Give the position of every malaria parasite.
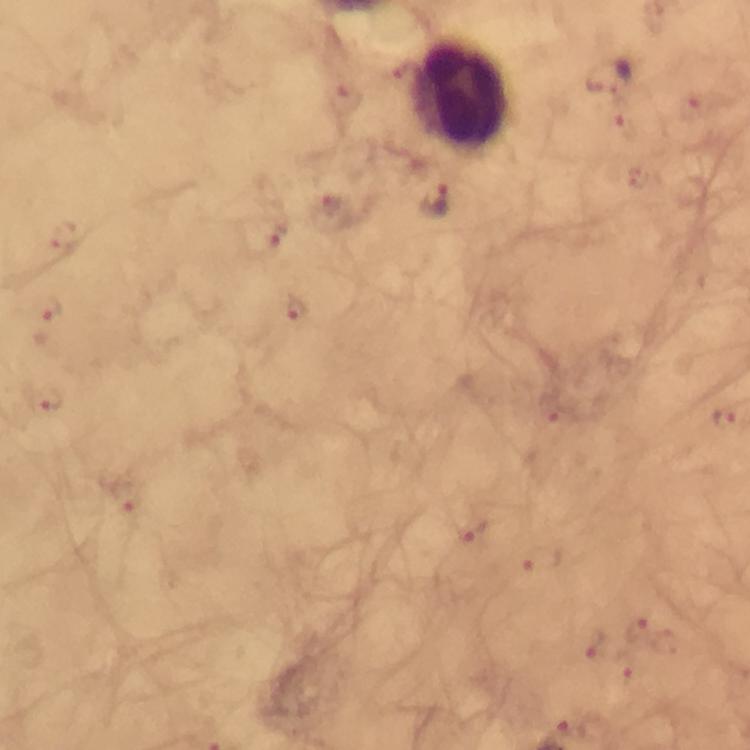

Approximate centers as (x, y) in pixels.
Malaria parasites: (405, 73), (611, 79), (345, 100), (693, 105), (626, 128), (639, 178), (433, 200), (331, 208), (277, 233), (64, 235), (296, 305), (47, 310), (47, 400), (549, 410), (726, 418), (124, 495), (475, 531), (542, 559), (637, 631), (593, 642), (627, 669), (570, 725).

{
  "magnification": "100x",
  "image_size": "750×750 pixels",
  "immersion_oil": "used",
  "preparation": "thick blood film",
  "cropped_from": "one field of view",
  "capture": "smartphone photograph through a microscope",
  "context": "from a malaria diagnostic workup",
  "leukocyte_locations": "approximate centers as (x, y) in pixels: (461, 94)",
  "stain": "Giemsa"
}